Outline each blood parasite and name the species.
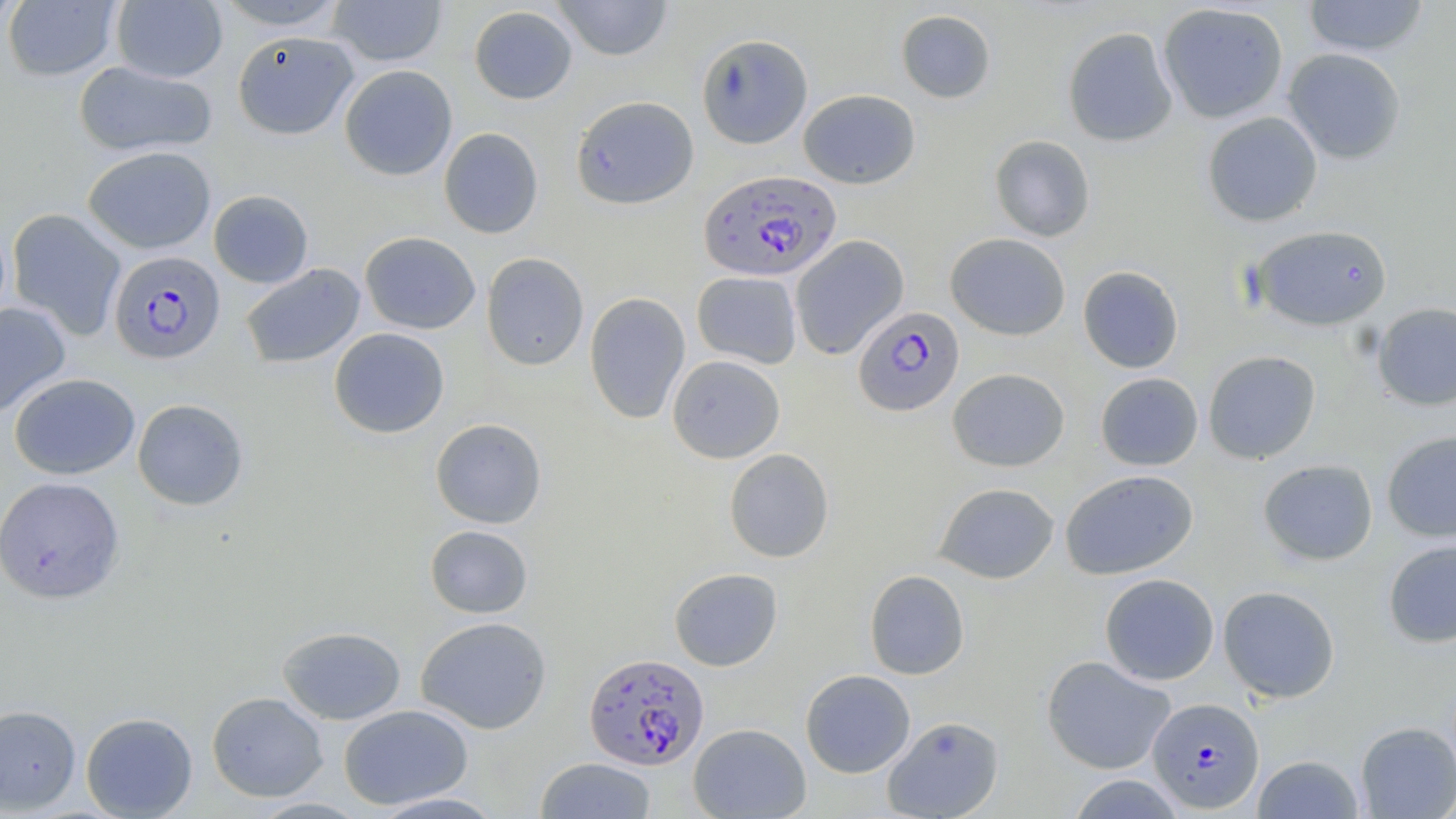

Approximate bounding boxes as (x1,y1)-(x2,y2) corner pairs in pixels.
Plasmodium falciparum-infected red blood cells: (699,170)-(842,281), (109,250)-(225,364), (853,305)-(964,416), (583,652)-(709,770), (1148,698)-(1264,812).
No Plasmodium ovale, Plasmodium malariae, Plasmodium vivax, Babesia divergens, or Trypanosoma brucei observed.

slide_level_diagnosis: Plasmodium falciparum
stain: May-Grünwald-Giemsa
uninfected_red_blood_cell_locations: 'approximate bounding boxes as (x1,y1)-(x2,y2) corner pairs in pixels: (0,0)-(23,35), (213,0)-(348,31), (552,0)-(674,61), (1302,0)-(1430,58), (2,1)-(121,82), (111,1)-(228,83), (327,1)-(448,67), (1157,3)-(1289,124), (469,5)-(577,105), (895,9)-(996,104), (1062,26)-(1178,147), (232,30)-(359,140), (696,33)-(813,149), (1282,48)-(1406,164), (74,61)-(217,157), (339,64)-(457,180), (798,89)-(920,189), (570,95)-(699,209), (1202,111)-(1323,227), (439,127)-(543,239), (989,135)-(1095,242), (83,146)-(216,254), (208,190)-(313,288), (7,208)-(126,341), (1250,224)-(1393,332), (360,231)-(481,334), (945,233)-(1071,340), (790,235)-(909,359), (481,252)-(589,370), (240,263)-(365,368), (1077,265)-(1184,373), (692,271)-(802,368), (584,292)-(690,424), (0,302)-(71,418), (1372,302)-(1456,411), (328,327)-(450,438), (1202,350)-(1321,464), (667,355)-(785,463), (947,368)-(1070,472), (1095,372)-(1204,471), (9,373)-(139,479), (132,398)-(249,511), (430,418)-(547,529), (1381,430)-(1456,542), (724,448)-(834,562), (1258,459)-(1378,566), (1060,469)-(1199,580), (0,476)-(125,604), (933,482)-(1060,584), (424,525)-(533,618), (1383,539)-(1456,648), (668,567)-(783,671), (864,570)-(969,680), (1099,573)-(1219,685), (1217,585)-(1340,702), (415,616)-(552,734), (277,626)-(406,725), (1041,655)-(1175,775), (800,669)-(916,778), (207,692)-(328,802), (0,704)-(81,814), (338,704)-(473,810), (81,711)-(198,818), (881,715)-(1005,819), (1355,722)-(1456,818), (688,723)-(811,819), (1252,754)-(1365,818), (535,757)-(657,818), (1066,775)-(1186,818), (368,791)-(507,818)'
field_of_view: single
image_size: 1456×819 pixels
modality: optical microscopy
preparation: thin blood film
magnification: 1000x